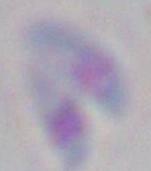

magnification = 1000x
modality = photomicrograph
identification = Toxoplasma gondii